Point out each leukocyte.
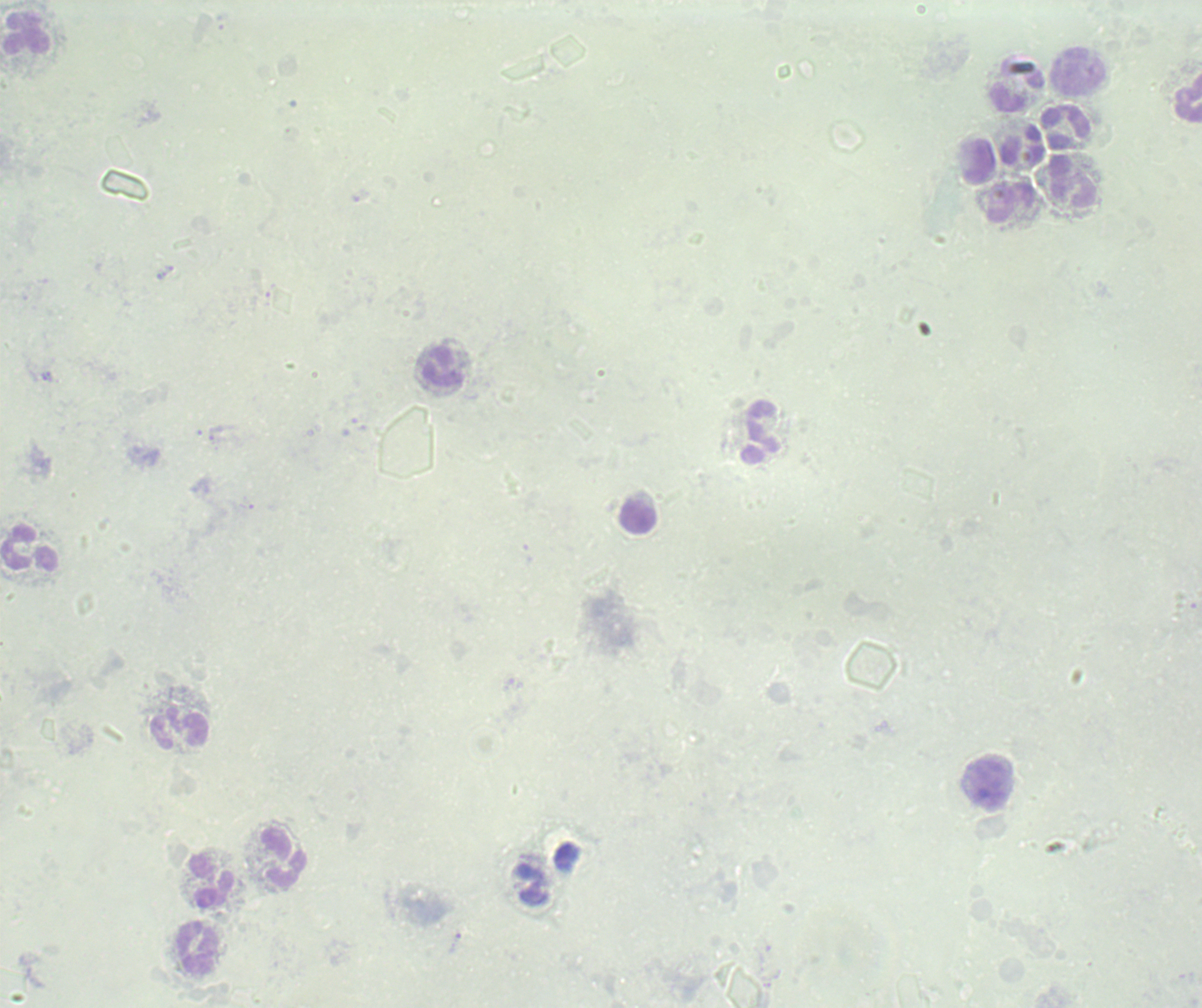

Approximate centers as (x, y) in pixels.
Leukocytes: (26, 35), (1078, 74), (1018, 86), (1188, 99), (1067, 129), (1024, 145), (978, 161), (1073, 182), (1009, 203), (443, 367), (761, 433), (638, 517), (29, 549), (179, 728), (990, 785), (283, 858), (210, 881), (198, 948).

{
  "image_size": "1202×1008 pixels",
  "background_quality": "unsatisfactory",
  "stain": "Romanowsky",
  "result": "no Plasmodium parasites seen",
  "field_of_view": "single",
  "preparation": "thick blood film",
  "magnification": "100x",
  "context": "previously used in a real diagnosis"
}